Locate every P. falciparum parasite and give its life-cycle stage, and locate every leukocyte and any debris.
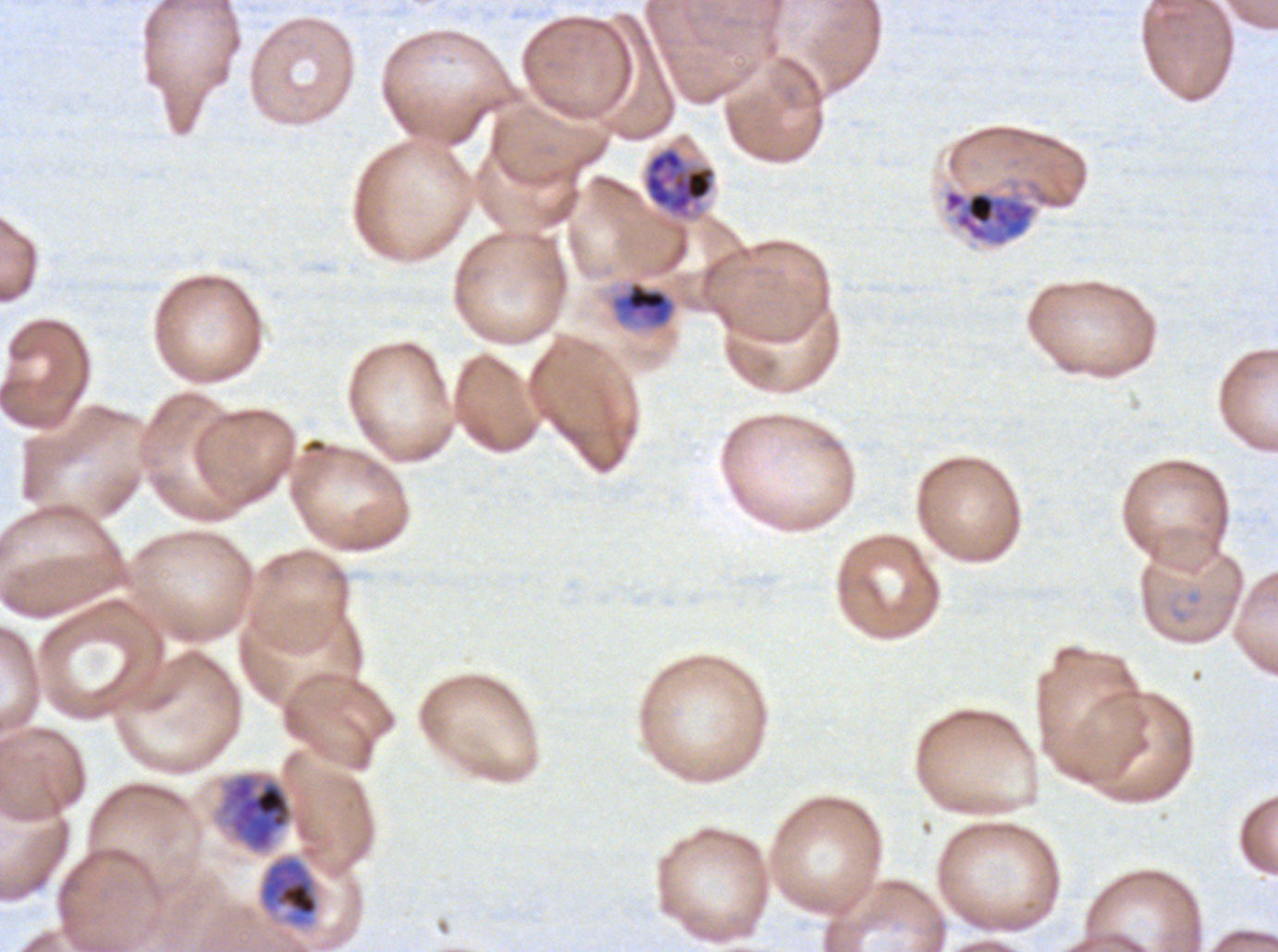

Approximate bounding boxes as (x1, y1, x2, y2) in pixels.
Mid trophozoites: (609, 280, 677, 329), (257, 853, 321, 929).
Late trophozoites: (642, 144, 718, 222), (943, 189, 1037, 246), (215, 770, 295, 855).
No rings, late-ring/early-trophozoite forms, early schizonts, late schizonts, segmenters, gametocytes, leukocytes, or debris observed.

stain = Giemsa
image size = 1278×952 pixels
field of view = sub-image separated from a larger composite
specimen = P. falciparum cultured ex vivo for 24 to 48 hours, from a patient in The Gambia
preparation = thin blood film
life-cycle stages observed = mid trophozoite, late trophozoite